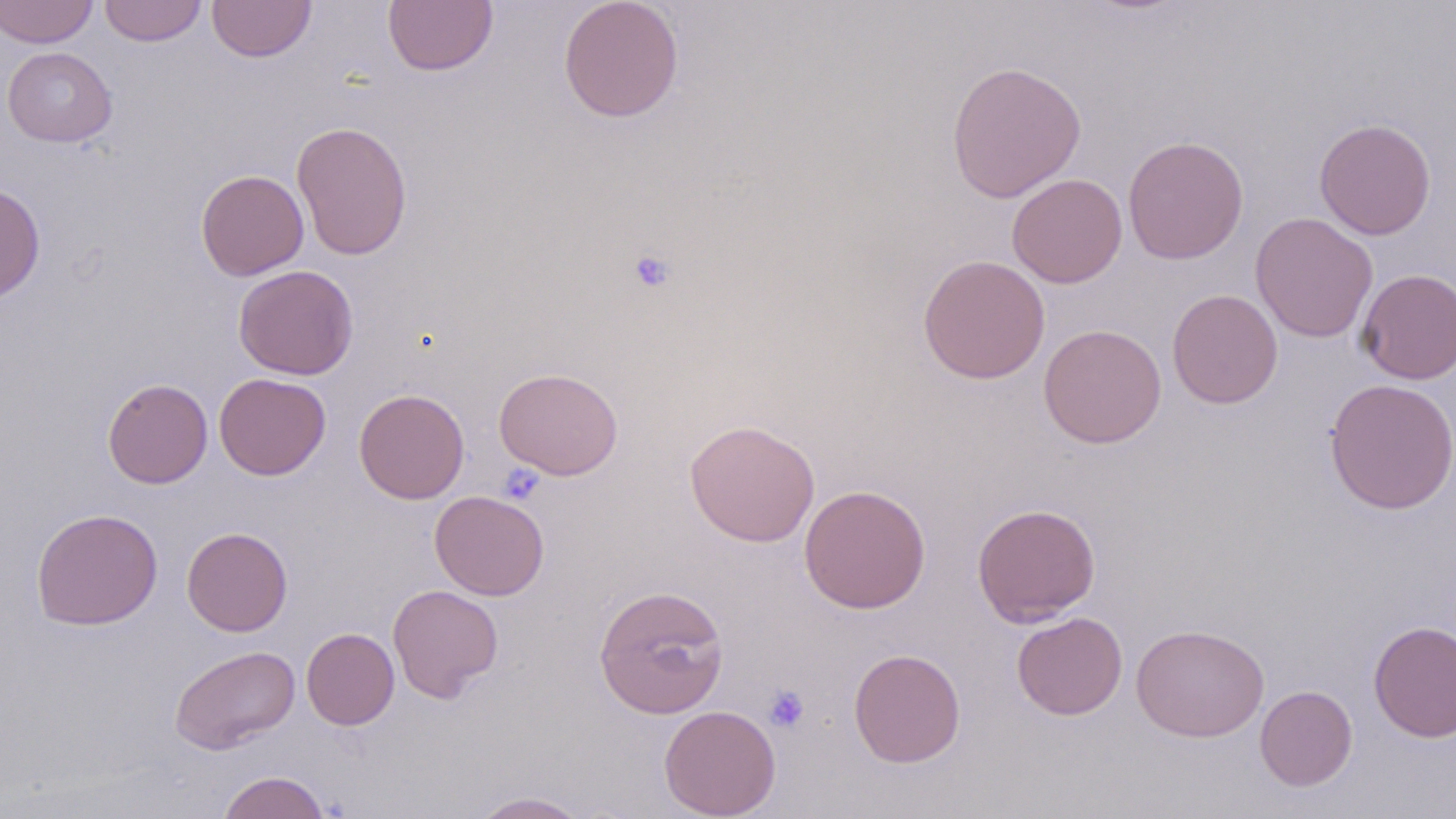
Approximate bounding boxes as named x1/y1/x2/y2 corners in pixels. Uninfected red blood cell locations: (x1=0, y1=0, x2=98, y2=48), (x1=99, y1=0, x2=206, y2=46), (x1=207, y1=0, x2=316, y2=62), (x1=382, y1=0, x2=498, y2=76), (x1=558, y1=0, x2=684, y2=123), (x1=1, y1=46, x2=117, y2=147), (x1=946, y1=59, x2=1087, y2=203), (x1=1314, y1=118, x2=1436, y2=240), (x1=291, y1=120, x2=413, y2=260), (x1=1122, y1=135, x2=1250, y2=265), (x1=196, y1=169, x2=309, y2=281), (x1=1007, y1=173, x2=1128, y2=288), (x1=0, y1=183, x2=45, y2=302), (x1=1250, y1=212, x2=1378, y2=343), (x1=917, y1=254, x2=1050, y2=384), (x1=233, y1=265, x2=359, y2=380), (x1=1357, y1=268, x2=1455, y2=384), (x1=1167, y1=288, x2=1283, y2=409), (x1=1039, y1=323, x2=1167, y2=449), (x1=494, y1=367, x2=624, y2=480), (x1=214, y1=373, x2=331, y2=480), (x1=102, y1=377, x2=213, y2=489), (x1=1324, y1=378, x2=1456, y2=514), (x1=353, y1=388, x2=469, y2=504), (x1=684, y1=419, x2=820, y2=547), (x1=799, y1=484, x2=931, y2=613), (x1=429, y1=490, x2=549, y2=601), (x1=972, y1=503, x2=1101, y2=626), (x1=30, y1=508, x2=163, y2=630), (x1=181, y1=526, x2=293, y2=636), (x1=593, y1=583, x2=729, y2=719), (x1=387, y1=584, x2=503, y2=702), (x1=1011, y1=612, x2=1128, y2=720), (x1=1368, y1=620, x2=1456, y2=743), (x1=1131, y1=623, x2=1269, y2=741), (x1=301, y1=627, x2=399, y2=730), (x1=170, y1=644, x2=300, y2=754), (x1=848, y1=648, x2=965, y2=768), (x1=1255, y1=685, x2=1357, y2=791), (x1=659, y1=705, x2=781, y2=818), (x1=217, y1=770, x2=332, y2=819), (x1=469, y1=791, x2=590, y2=819). Platelet locations: (x1=628, y1=248, x2=676, y2=294), (x1=499, y1=463, x2=546, y2=506), (x1=763, y1=685, x2=809, y2=733). Slide-level diagnosis: negative for blood parasites. Image is 1456×819 pixels. May-Grünwald-Giemsa-stained preparation. Optical microscopy. One field of a larger specimen. Thin blood smear. Captured at 1000x magnification.